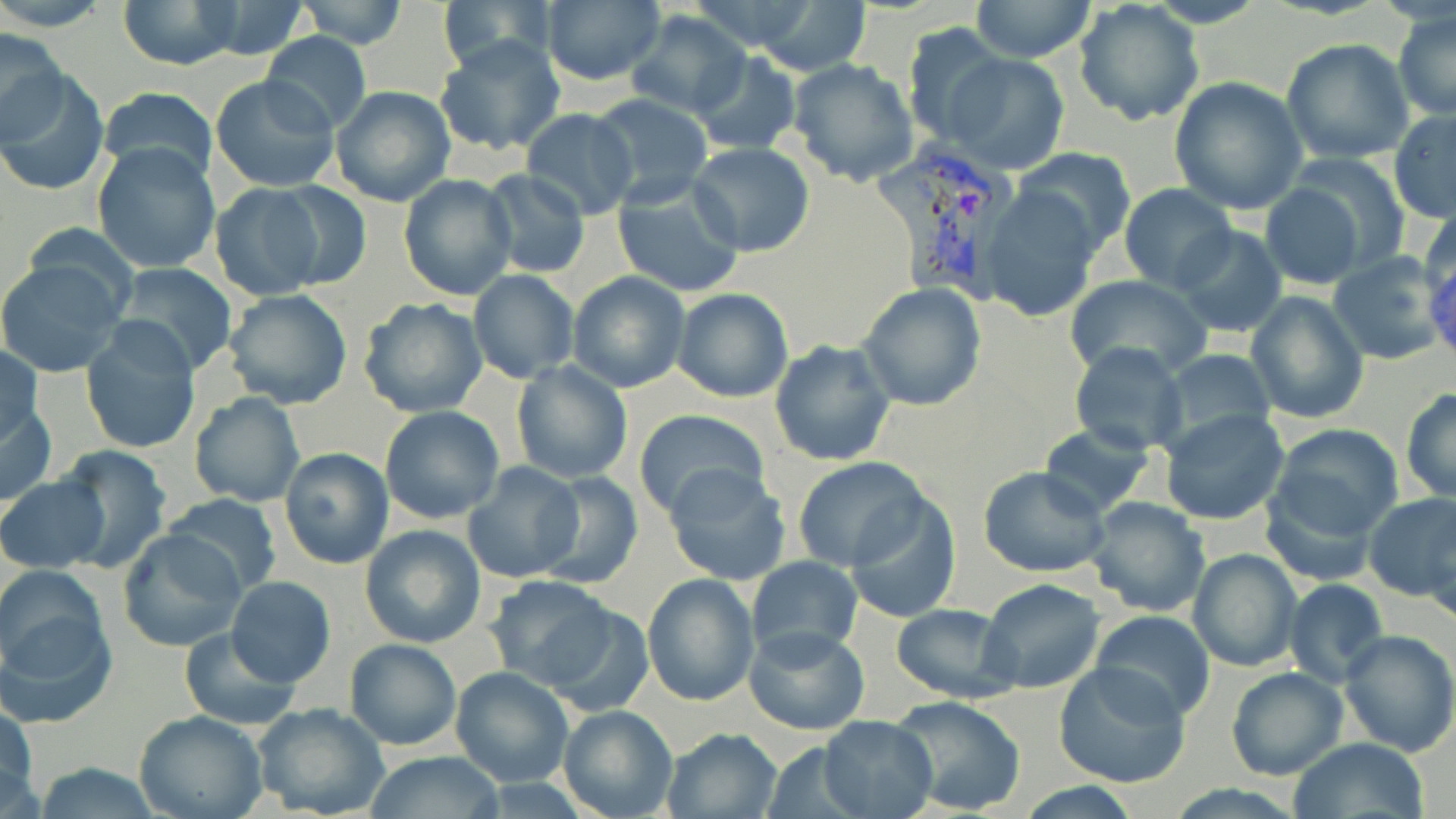
slide_level_diagnosis: Plasmodium vivax
magnification: 1000x
uninfected_red_blood_cell_locations: 'approximate bounding boxes as named x1/y1/x2/y2 corners in pixels: (x1=0, y1=0, x2=113, y2=32), (x1=436, y1=0, x2=561, y2=72), (x1=684, y1=0, x2=826, y2=54), (x1=971, y1=0, x2=1096, y2=63), (x1=1141, y1=0, x2=1269, y2=27), (x1=118, y1=1, x2=245, y2=69), (x1=291, y1=1, x2=412, y2=49), (x1=537, y1=1, x2=667, y2=86), (x1=185, y1=2, x2=319, y2=61), (x1=751, y1=2, x2=872, y2=74), (x1=1073, y1=3, x2=1205, y2=126), (x1=1392, y1=8, x2=1455, y2=123), (x1=624, y1=11, x2=752, y2=120), (x1=901, y1=23, x2=1006, y2=146), (x1=0, y1=27, x2=68, y2=144), (x1=260, y1=31, x2=372, y2=134), (x1=435, y1=34, x2=566, y2=157), (x1=1280, y1=37, x2=1415, y2=165), (x1=690, y1=51, x2=802, y2=155), (x1=944, y1=52, x2=1069, y2=175), (x1=787, y1=57, x2=919, y2=186), (x1=2, y1=68, x2=107, y2=198), (x1=210, y1=74, x2=339, y2=194), (x1=1169, y1=77, x2=1310, y2=214), (x1=329, y1=85, x2=455, y2=207), (x1=98, y1=88, x2=217, y2=187), (x1=586, y1=92, x2=713, y2=209), (x1=1389, y1=108, x2=1456, y2=223), (x1=521, y1=111, x2=638, y2=220), (x1=92, y1=140, x2=220, y2=272), (x1=687, y1=143, x2=817, y2=256), (x1=1013, y1=147, x2=1136, y2=257), (x1=1279, y1=155, x2=1412, y2=279), (x1=478, y1=169, x2=590, y2=279), (x1=398, y1=174, x2=519, y2=300), (x1=611, y1=180, x2=745, y2=300), (x1=257, y1=181, x2=373, y2=292), (x1=207, y1=182, x2=328, y2=302), (x1=1258, y1=182, x2=1367, y2=289), (x1=1119, y1=185, x2=1235, y2=293), (x1=979, y1=186, x2=1103, y2=322), (x1=1418, y1=200, x2=1456, y2=309), (x1=1172, y1=223, x2=1288, y2=338), (x1=1327, y1=251, x2=1448, y2=366), (x1=0, y1=258, x2=129, y2=379), (x1=111, y1=264, x2=239, y2=375), (x1=469, y1=270, x2=578, y2=383), (x1=567, y1=270, x2=691, y2=392), (x1=1064, y1=273, x2=1212, y2=382), (x1=858, y1=284, x2=986, y2=411), (x1=671, y1=288, x2=794, y2=403), (x1=222, y1=290, x2=354, y2=410), (x1=1243, y1=291, x2=1369, y2=425), (x1=357, y1=297, x2=489, y2=420), (x1=80, y1=319, x2=202, y2=455), (x1=769, y1=340, x2=896, y2=468), (x1=0, y1=342, x2=42, y2=451), (x1=1069, y1=342, x2=1186, y2=455), (x1=1160, y1=348, x2=1275, y2=452), (x1=511, y1=360, x2=632, y2=484), (x1=1400, y1=386, x2=1456, y2=503), (x1=1, y1=390, x2=57, y2=510), (x1=189, y1=392, x2=306, y2=509), (x1=379, y1=406, x2=505, y2=525), (x1=1160, y1=408, x2=1290, y2=528), (x1=634, y1=410, x2=769, y2=522), (x1=1267, y1=423, x2=1405, y2=541), (x1=1038, y1=425, x2=1154, y2=517), (x1=53, y1=445, x2=173, y2=573), (x1=279, y1=447, x2=395, y2=569), (x1=792, y1=457, x2=929, y2=571), (x1=462, y1=461, x2=585, y2=584), (x1=662, y1=463, x2=792, y2=585), (x1=977, y1=466, x2=1110, y2=579), (x1=535, y1=471, x2=643, y2=589), (x1=0, y1=473, x2=110, y2=573), (x1=63, y1=486, x2=199, y2=626), (x1=162, y1=492, x2=283, y2=597), (x1=1363, y1=492, x2=1456, y2=601), (x1=843, y1=494, x2=961, y2=622), (x1=1084, y1=495, x2=1211, y2=616), (x1=359, y1=524, x2=488, y2=649), (x1=118, y1=528, x2=246, y2=654), (x1=1423, y1=530, x2=1454, y2=630), (x1=1188, y1=548, x2=1303, y2=672), (x1=745, y1=555, x2=864, y2=661), (x1=0, y1=564, x2=115, y2=719), (x1=641, y1=574, x2=759, y2=706), (x1=485, y1=575, x2=623, y2=693), (x1=224, y1=576, x2=336, y2=689), (x1=1282, y1=577, x2=1389, y2=686), (x1=978, y1=578, x2=1107, y2=695), (x1=535, y1=599, x2=656, y2=715), (x1=890, y1=602, x2=1015, y2=703), (x1=1088, y1=610, x2=1217, y2=720), (x1=743, y1=626, x2=870, y2=735), (x1=180, y1=628, x2=302, y2=729), (x1=1337, y1=628, x2=1456, y2=758), (x1=344, y1=638, x2=462, y2=750), (x1=1053, y1=663, x2=1191, y2=789), (x1=450, y1=666, x2=573, y2=787), (x1=1226, y1=667, x2=1349, y2=781), (x1=889, y1=695, x2=1029, y2=817), (x1=0, y1=697, x2=39, y2=818), (x1=252, y1=703, x2=391, y2=819), (x1=557, y1=704, x2=678, y2=819), (x1=135, y1=711, x2=269, y2=819), (x1=819, y1=715, x2=938, y2=819), (x1=661, y1=728, x2=782, y2=818), (x1=1288, y1=737, x2=1428, y2=819), (x1=758, y1=740, x2=876, y2=819), (x1=361, y1=751, x2=507, y2=819), (x1=29, y1=762, x2=161, y2=819), (x1=1013, y1=781, x2=1148, y2=817)'
stain: May-Grünwald-Giemsa
preparation: thin blood smear
field_of_view: one of a larger specimen
modality: optical microscopy
image_size: 1456×819 pixels
plasmodium_vivax_infected_red_blood_cell_locations: 'approximate bounding boxes as named x1/y1/x2/y2 corners in pixels: (x1=875, y1=135, x2=1024, y2=309)'